Classify the preparation.
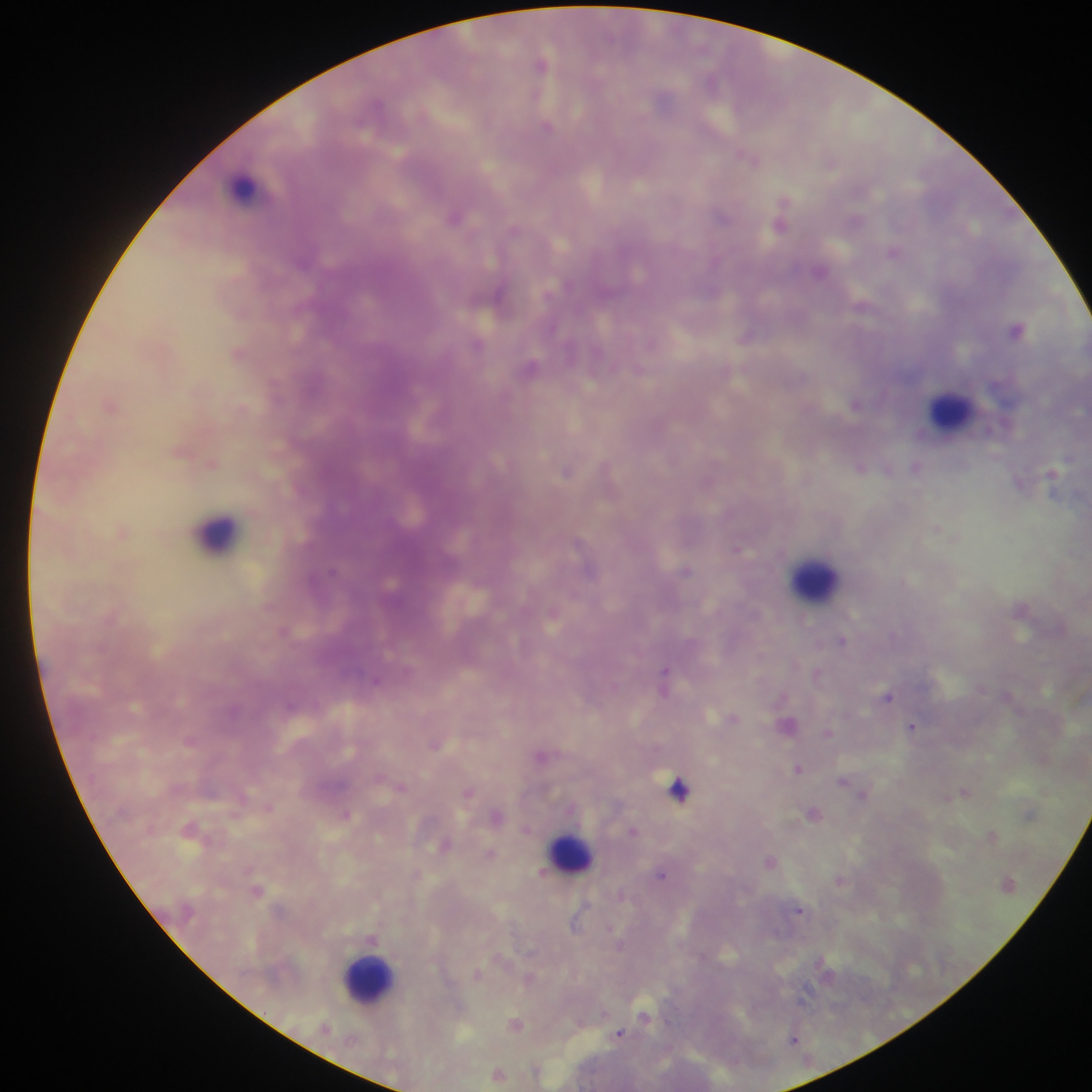

This is a thick smear.

Approximate centers as [x, y] in pixels. Malaria parasite locations: [541, 64], [547, 126], [750, 159], [831, 163], [722, 214], [455, 217], [781, 223], [513, 228], [894, 252], [1017, 330], [746, 335], [651, 343], [477, 344], [530, 367], [639, 370], [212, 463], [860, 467], [566, 471], [738, 549], [687, 570], [284, 631], [842, 640], [664, 673], [817, 673], [376, 682], [887, 696], [913, 726], [827, 734], [190, 740], [436, 744], [540, 755], [798, 768], [843, 781], [401, 786], [679, 788], [469, 792], [965, 792], [813, 813], [347, 815], [633, 831], [992, 836], [444, 846], [491, 854], [770, 862], [662, 874], [840, 880], [258, 891], [799, 910], [645, 1016], [515, 1024], [619, 1033], [793, 1039], [499, 1074]. Leukocyte locations: [248, 188], [949, 411], [219, 533], [814, 577], [569, 851], [370, 976]. Image is 1092×1092 pixels. Single field of view. Sample from Ghana. Photographed through a microscope with a mobile-phone camera.